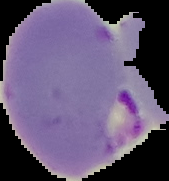
image_size: 169×181 pixels
malaria_status: parasitized
preparation: thin blood smear
image_type: segmented cell region with the area outside set to black